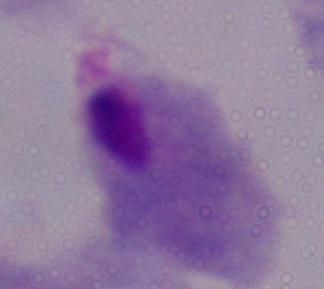

identification = trichomonad
magnification = 1000x
modality = photomicrograph